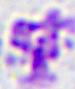
magnification = 400x
identification = white blood cell
modality = micrograph